Assess the morphology of the erythrocytes.
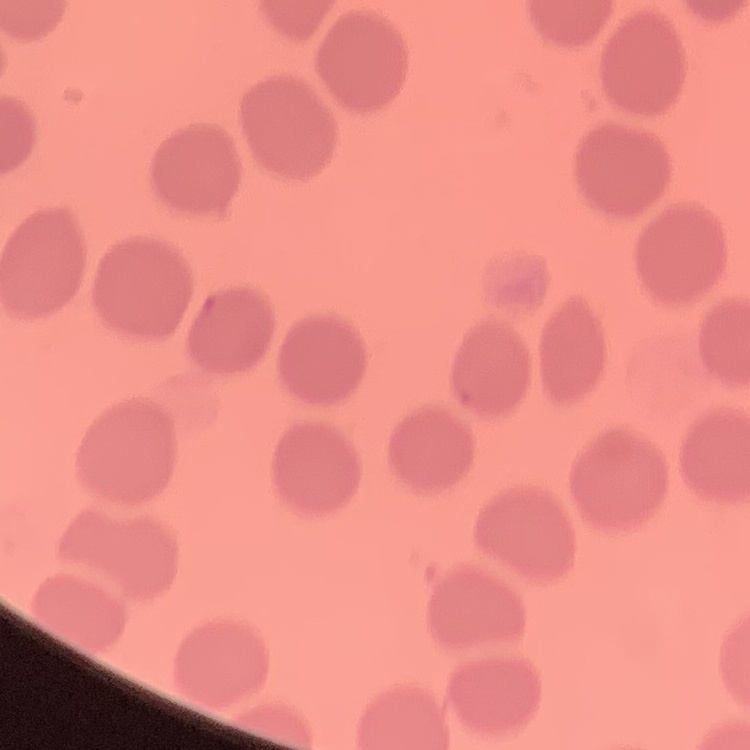

No rouleaux formation.

Stained with either Field's or Giemsa. One tile cut from a larger photomicrograph. Thin blood film.